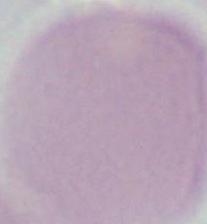

{
  "modality": "micrograph",
  "magnification": "1000x",
  "identification": "red blood cell"
}